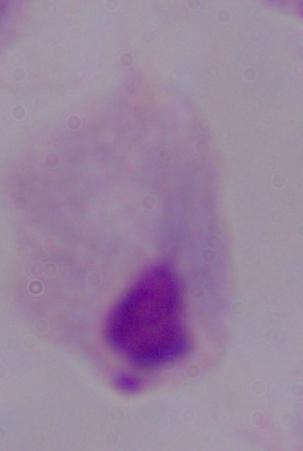
Summary:
  - Identification: trichomonad
  - Magnification: 1000x
  - Modality: photomicrograph